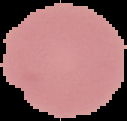

The area outside the segmented cell region is set to black. Malaria status: uninfected. Image is 127×121 pixels. From a thin blood film.